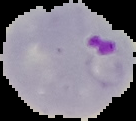
image type = cell region segmented out of the field of view; surrounding area masked to black
preparation = thin blood smear
result = malaria parasites identified
image size = 136×121 pixels